Outline every parasitised red blood cell.
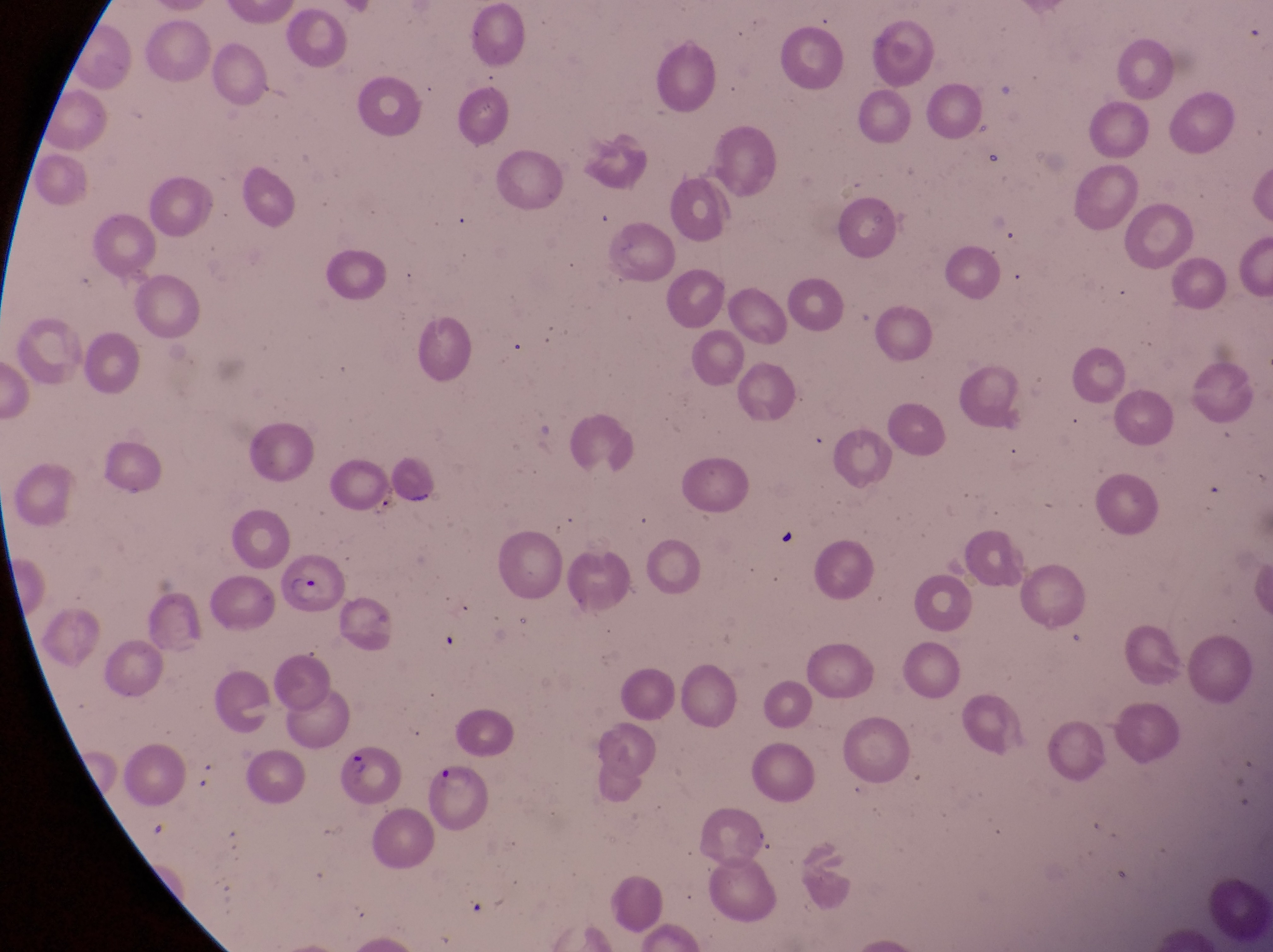
Approximate bounding boxes as (left, top, right, bottom) in pixels.
Parasitised red blood cells: (278, 552, 347, 619), (333, 741, 396, 807), (423, 765, 497, 834).

Single field of view. At a magnification of 1000x. Thin blood smear. Photographed through the eyepiece of an Olympus CX-23 microscope with a smartphone camera. Sample from Uganda. Image is 1273×952 pixels.